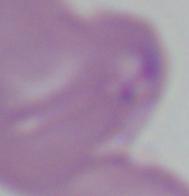

Summary:
  - Modality: photomicrograph
  - Identification: Babesia
  - Magnification: 1000x